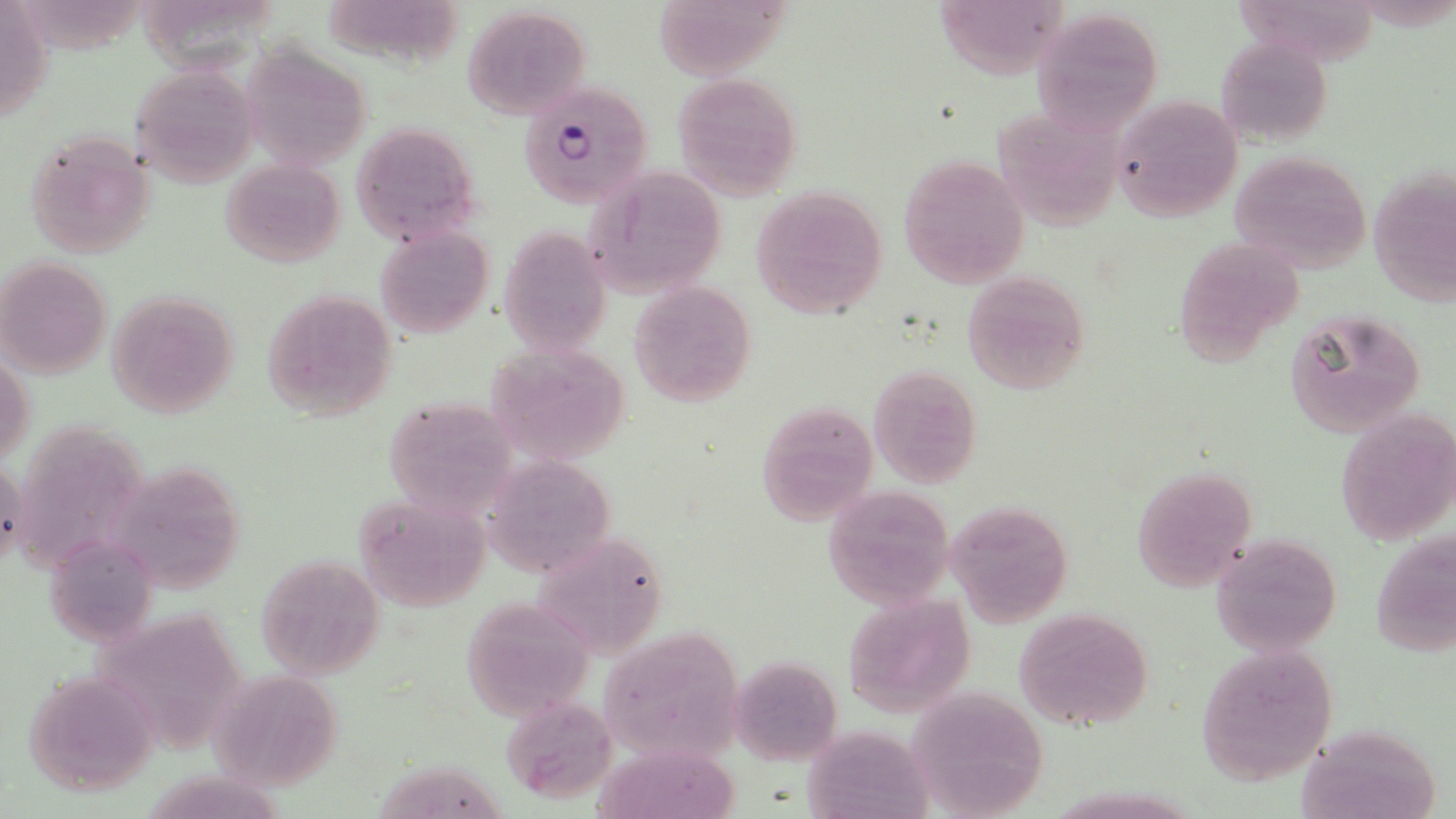

slide-level diagnosis = Plasmodium falciparum
magnification = 1000x
modality = optical microscopy
field of view = one of a larger specimen
preparation = thin blood film
image size = 1456×819 pixels
uninfected red blood cell locations = approximate bounding boxes as [x1, y1, x2, y2] in pixels: [2, 0, 53, 128], [31, 0, 153, 62], [330, 0, 461, 72], [933, 0, 1067, 78], [1233, 0, 1382, 72], [658, 1, 804, 82], [153, 5, 283, 79], [462, 6, 591, 119], [1034, 7, 1165, 132], [1216, 36, 1333, 148], [241, 45, 371, 173], [131, 66, 258, 187], [671, 71, 802, 201], [1110, 96, 1243, 223], [995, 111, 1122, 241], [351, 122, 481, 245], [24, 130, 155, 258], [1228, 151, 1373, 275], [897, 154, 1029, 289], [220, 159, 346, 269], [584, 166, 728, 298], [1368, 166, 1455, 308], [750, 185, 888, 317], [500, 226, 612, 354], [374, 227, 494, 339], [1174, 235, 1305, 362], [1, 255, 113, 380], [961, 271, 1090, 393], [630, 280, 755, 407], [264, 288, 398, 420], [104, 291, 240, 418], [1284, 309, 1428, 437], [487, 341, 631, 465], [1, 351, 33, 469], [869, 365, 981, 487], [382, 394, 517, 518], [756, 399, 878, 525], [1334, 407, 1456, 546], [4, 421, 146, 580], [489, 455, 616, 581], [126, 465, 244, 598], [1130, 467, 1256, 589], [822, 483, 955, 608], [356, 493, 494, 612], [945, 501, 1071, 625], [531, 525, 668, 666], [1372, 526, 1454, 661], [1211, 531, 1343, 658], [51, 543, 168, 649], [254, 556, 384, 679], [845, 592, 976, 717], [480, 594, 601, 724], [1013, 608, 1154, 732], [109, 613, 243, 755], [597, 626, 743, 765], [1194, 646, 1337, 784], [731, 655, 842, 767], [20, 669, 160, 795], [207, 669, 346, 792], [903, 685, 1050, 818], [503, 695, 618, 803], [1295, 722, 1446, 819], [798, 728, 928, 819], [595, 743, 743, 818], [382, 764, 520, 819], [143, 767, 299, 819]
stain = May-Grünwald-Giemsa
Plasmodium falciparum-infected red blood cell locations = approximate bounding boxes as [x1, y1, x2, y2] in pixels: [518, 81, 653, 207]